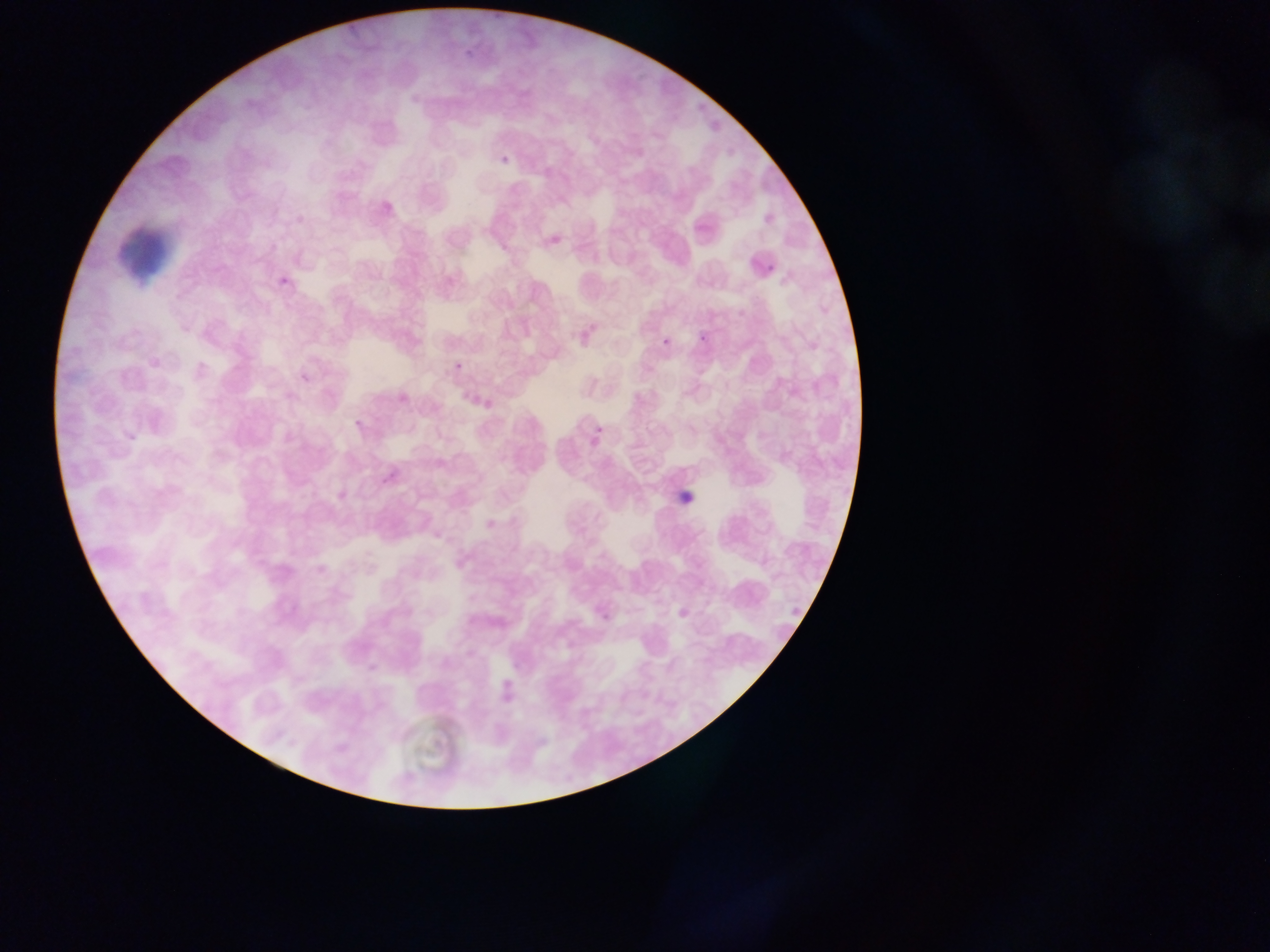
Approximate bounding boxes as (left, top, right, bottom) in pixels. Leukocyte locations: (109, 218, 182, 287). Plasmodium parasite locations: (464, 51, 477, 61), (501, 156, 509, 164), (297, 215, 305, 223), (767, 258, 780, 275), (276, 273, 289, 287), (695, 332, 714, 343), (455, 363, 463, 372), (354, 419, 363, 428), (595, 426, 603, 433), (597, 612, 615, 623) | approximate (x, y) pixel centers of objects too small to bound: (666, 342). Sample from Ghana. Single field of view. Image is 1270×952 pixels. Thin blood smear. Mobile-phone photograph taken through the microscope.